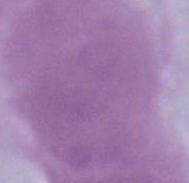 Micrograph. Captured at 1000x magnification. A red blood cell is seen.